Outline each Babesia divergens-infected red blood cell.
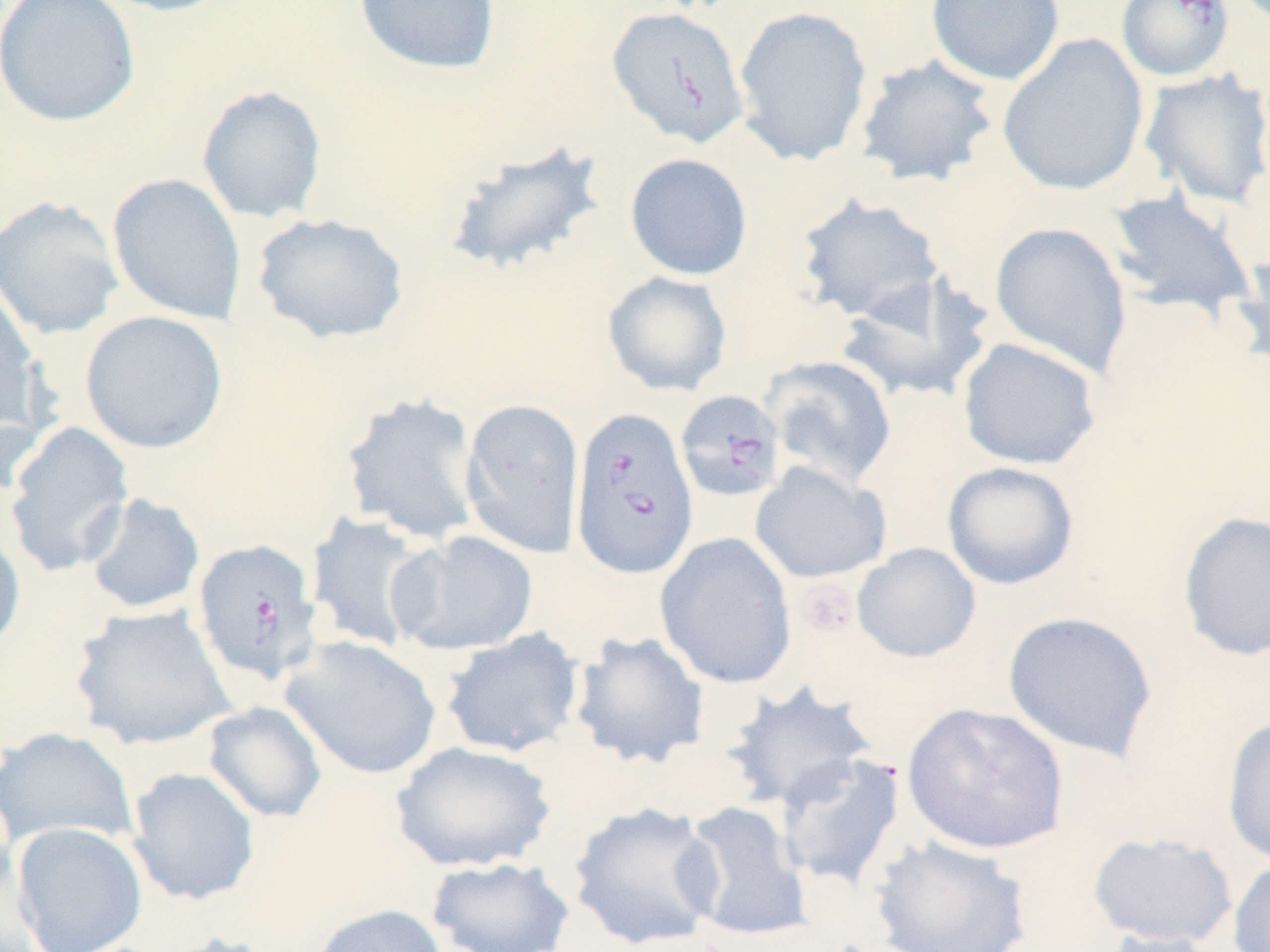
Approximate bounding boxes as (x1, y1, x2, y2) in pixels.
Babesia divergens-infected red blood cells: (1115, 0, 1235, 83), (607, 6, 749, 149), (675, 390, 784, 503), (569, 406, 700, 580), (191, 538, 325, 688).

{
  "slide_level_diagnosis": "Babesia divergens",
  "stain": "May-Grünwald-Giemsa",
  "modality": "light microscopy",
  "platelet_locations": "approximate bounding boxes as (x1, y1, x2, y2) in pixels: (793, 579, 860, 638)",
  "field_of_view": "single",
  "uninfected_red_blood_cell_locations": "approximate bounding boxes as (x1, y1, x2, y2) in pixels: (0, 0, 140, 127), (94, 0, 239, 17), (354, 0, 501, 75), (926, 0, 1065, 86), (732, 5, 873, 168), (996, 33, 1150, 197), (854, 54, 1000, 187), (1139, 68, 1270, 209), (196, 85, 328, 224), (444, 138, 609, 277), (624, 153, 753, 281), (107, 173, 248, 326), (1103, 188, 1258, 320), (793, 192, 947, 323), (0, 195, 125, 340), (251, 212, 410, 346), (989, 221, 1133, 378), (1232, 246, 1270, 379), (602, 271, 733, 396), (835, 275, 995, 404), (0, 283, 45, 435), (79, 310, 228, 455), (957, 336, 1102, 470), (761, 355, 897, 489), (340, 391, 485, 546), (460, 398, 585, 559), (3, 421, 136, 578), (750, 461, 892, 584), (942, 461, 1079, 590), (81, 492, 206, 614), (1176, 510, 1270, 662), (305, 511, 438, 652), (0, 526, 26, 657), (387, 530, 539, 655), (653, 532, 799, 690), (851, 543, 981, 664), (69, 604, 238, 751), (1002, 611, 1159, 762), (438, 628, 585, 759), (570, 631, 711, 770), (280, 635, 442, 780), (719, 681, 881, 811), (202, 701, 328, 824), (902, 702, 1069, 855), (1221, 716, 1270, 866), (1, 727, 139, 851), (391, 741, 557, 873), (774, 752, 906, 892), (125, 766, 261, 906), (677, 800, 814, 943), (567, 802, 725, 950), (10, 821, 149, 952), (1087, 831, 1238, 949), (869, 835, 1034, 952), (425, 856, 576, 952), (1228, 857, 1270, 952), (310, 903, 450, 952), (1096, 928, 1224, 952), (154, 932, 282, 952)",
  "preparation": "thin blood smear",
  "image_size": "1270×952 pixels",
  "magnification": "1000x"
}